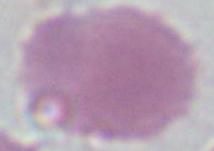
Summary:
  - Modality: micrograph
  - Identification: erythrocyte
  - Magnification: 1000x